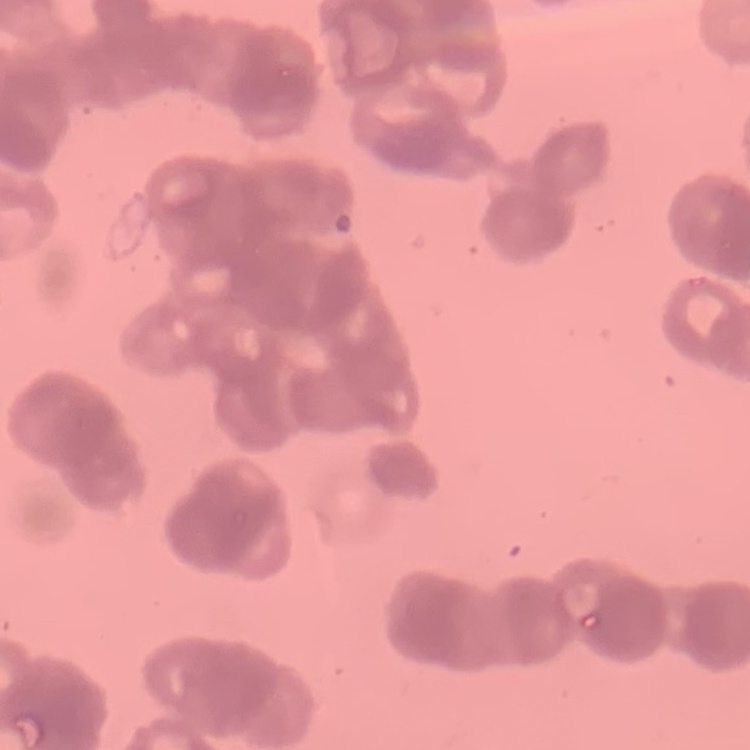 The red blood cells show rouleaux formation. Square crop of a larger photomicrograph. Thin peripheral smear. Field's or Giemsa stain.